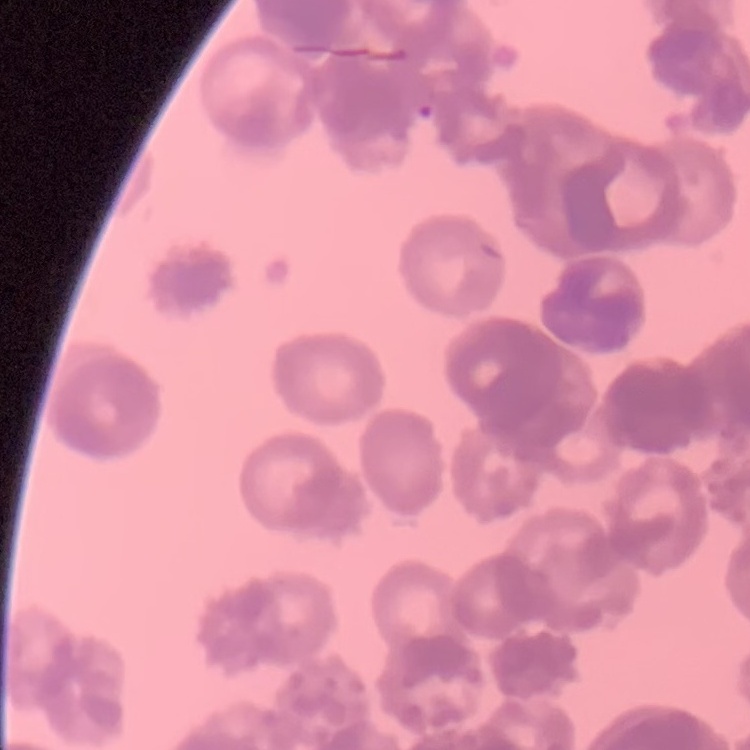
The erythrocytes exhibit rouleaux formation. Stained with either Field's or Giemsa. Thin blood film. Square crop of a larger photomicrograph.